Comment on the morphology of the erythrocytes.
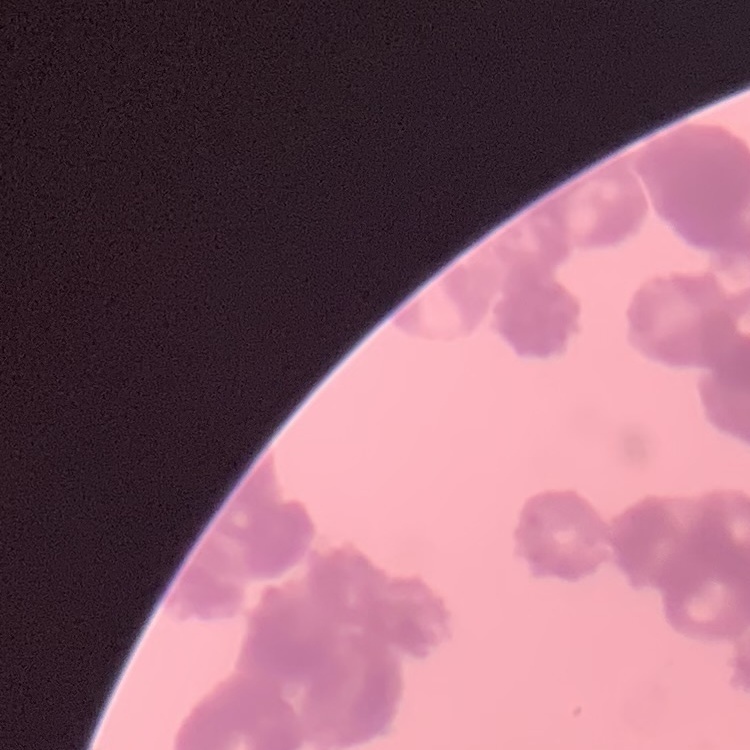
They show rouleaux formation.

image_type: square crop of a larger photomicrograph
stain: Field's or Giemsa
preparation: thin peripheral smear